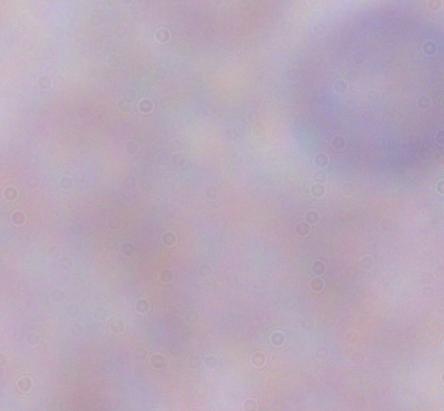
modality = photomicrograph
magnification = 1000x
identification = trypanosome